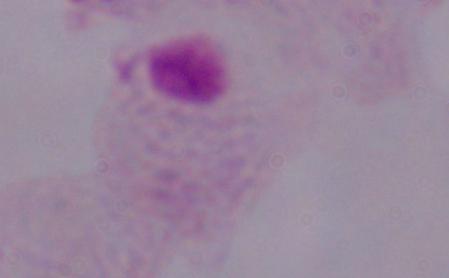

{
  "identification": "trichomonad",
  "magnification": "1000x",
  "modality": "micrograph"
}